Mark where leukocytes are.
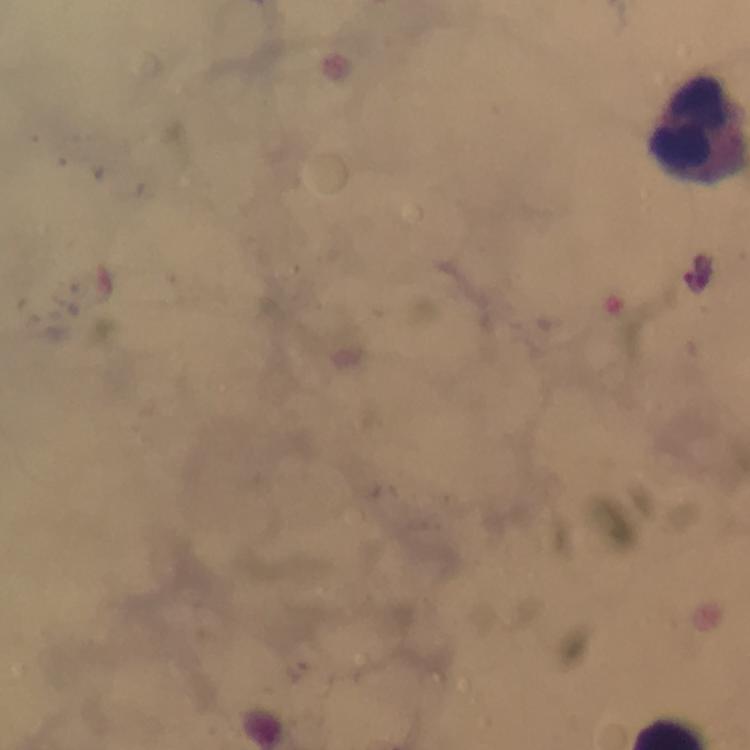

Approximate centers as (x, y) in pixels.
Leukocytes: (693, 122).

Summary:
  - Malaria parasite locations: (698, 271)
  - Immersion oil: used
  - Preparation: thick smear
  - Context: from a diagnostic examination for malaria
  - Cropped from: a single field of view
  - Stain: Giemsa
  - Magnification: 100x
  - Image size: 750×750 pixels
  - Capture: smartphone mounted on the microscope